Name the blood parasite species.
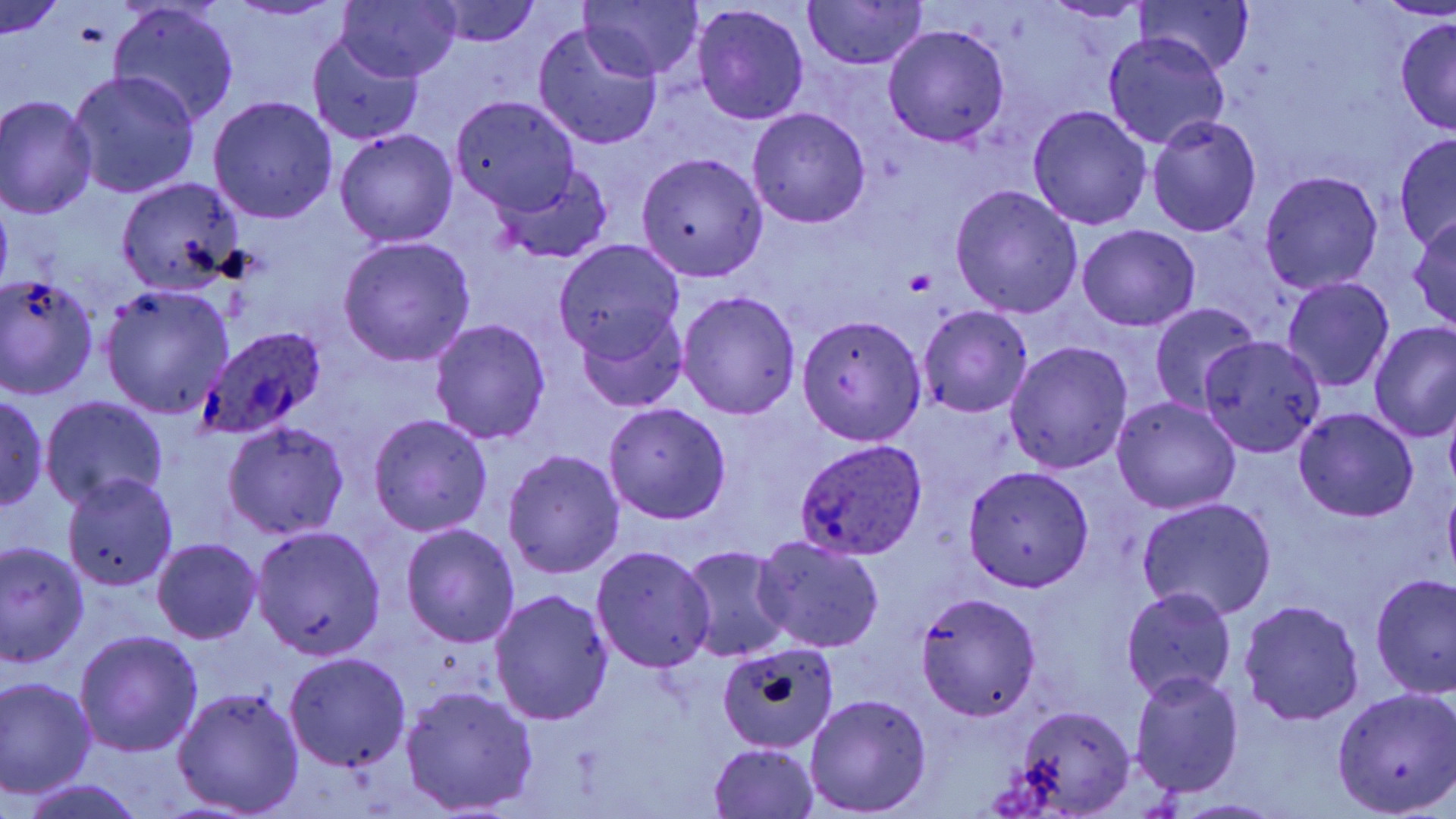
Plasmodium ovale.

Approximate bounding boxes as (x1, y1, x2, y2) in pixels. Platelet locations: (905, 269, 935, 296). Uninfected red blood cell locations: (222, 0, 347, 20), (335, 0, 461, 84), (1134, 0, 1257, 77), (424, 2, 541, 48), (580, 2, 705, 81), (802, 2, 930, 70), (1044, 2, 1152, 23), (1, 3, 67, 40), (108, 4, 241, 126), (692, 4, 810, 125), (1394, 17, 1456, 136), (531, 21, 663, 150), (883, 25, 1010, 146), (306, 31, 426, 143), (1103, 33, 1230, 149), (67, 69, 201, 197), (0, 95, 97, 218), (208, 97, 338, 224), (450, 97, 582, 217), (1026, 105, 1152, 229), (747, 108, 870, 228), (1146, 115, 1261, 237), (334, 128, 459, 248), (1394, 134, 1456, 249), (634, 152, 769, 281), (493, 160, 611, 265), (1260, 170, 1383, 295), (116, 176, 244, 293), (950, 184, 1083, 319), (1408, 216, 1456, 329), (1077, 224, 1201, 331), (337, 237, 476, 366), (556, 240, 684, 364), (1, 274, 97, 396), (1281, 278, 1395, 393), (99, 285, 234, 417), (676, 290, 801, 419), (1149, 302, 1259, 416), (917, 306, 1033, 418), (574, 307, 689, 413), (798, 316, 927, 447), (428, 319, 551, 443), (1369, 323, 1456, 443), (1201, 337, 1324, 455), (1004, 342, 1133, 474), (0, 394, 47, 510), (40, 396, 170, 510), (1110, 396, 1241, 515), (602, 402, 731, 523), (1444, 404, 1456, 495), (1292, 408, 1419, 523), (368, 413, 492, 536), (223, 422, 350, 543), (501, 449, 625, 580), (961, 465, 1095, 591), (63, 474, 178, 593), (1442, 490, 1456, 578), (1138, 497, 1277, 621), (400, 523, 521, 648), (251, 526, 387, 659), (751, 535, 885, 654), (152, 539, 263, 644), (1, 541, 90, 665), (590, 545, 717, 673), (680, 546, 792, 662), (1371, 573, 1456, 699), (1120, 587, 1238, 704), (489, 588, 613, 727), (917, 591, 1041, 721), (1238, 598, 1366, 726), (74, 630, 203, 759), (716, 642, 841, 752), (285, 651, 411, 772), (1130, 670, 1245, 798), (1, 675, 97, 800), (173, 686, 305, 816), (401, 686, 539, 814), (1331, 686, 1456, 814), (804, 693, 932, 816), (1013, 706, 1134, 817), (708, 742, 822, 818), (15, 778, 148, 819), (1172, 798, 1286, 818). Plasmodium ovale-infected red blood cell locations: (200, 328, 328, 439), (794, 440, 928, 561). Single field of view. Thin blood film. Image is 1456×819 pixels. 1000x magnification. Light microscopy. May-Grünwald-Giemsa-stained preparation.